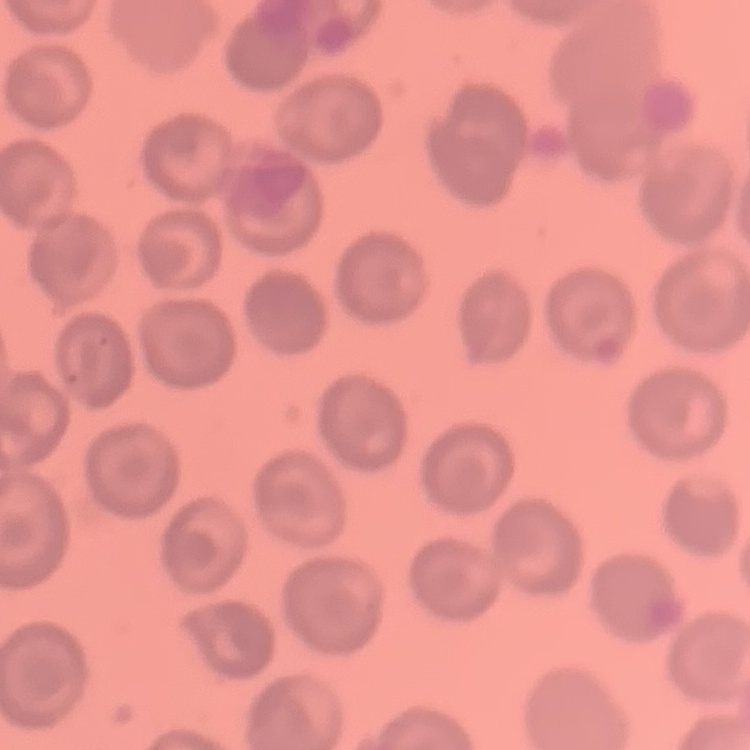

erythrocyte morphology = no rouleaux formation
preparation = thin blood film
image type = one tile cut from a larger photomicrograph
stain = Field's or Giemsa